State which parasite is depicted.
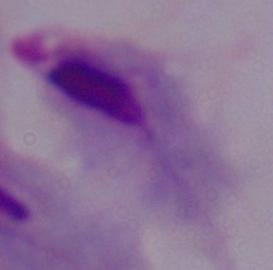

A trichomonad.

Photomicrograph. Captured at 1000x magnification.